Describe the morphology of the red blood cells.
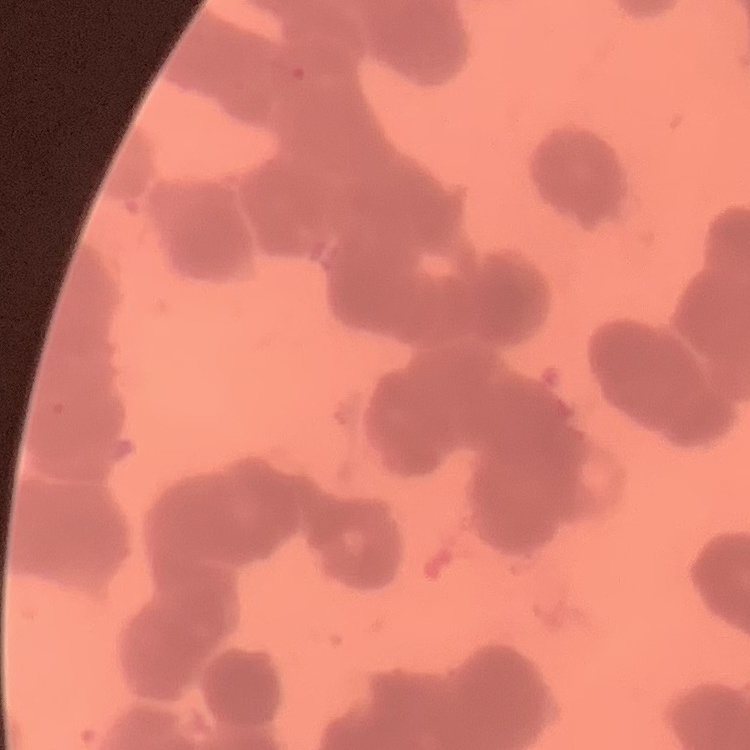
They show rouleaux formation.

image type = square crop of a larger photomicrograph
stain = Field's or Giemsa
preparation = thin blood smear